Evaluate for Plasmodium parasites.
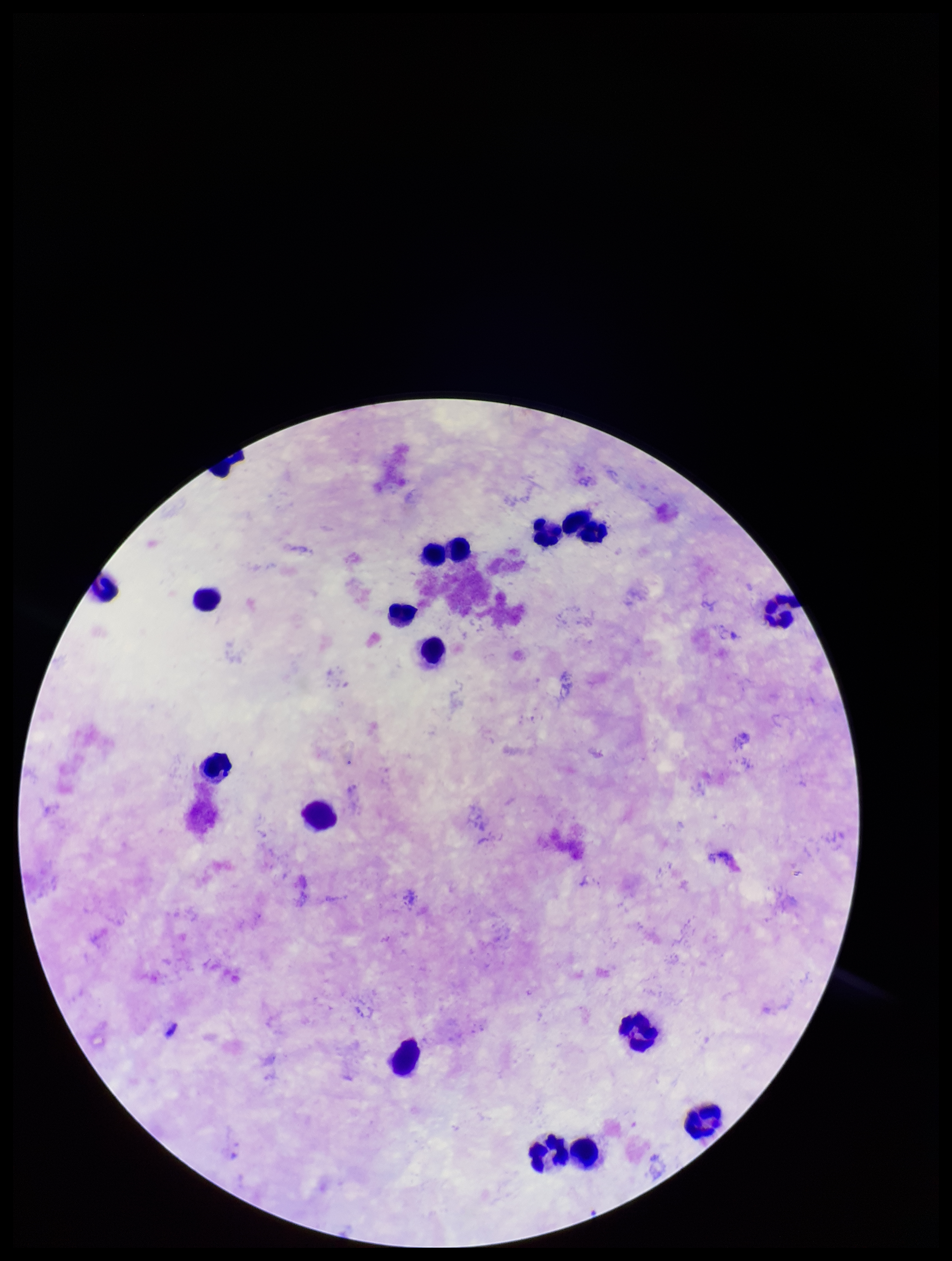
None seen.

Parasite count: 0. Leukocyte count: 16. Photographed through the microscope eyepiece with a smartphone camera. Single field of view. Preparation: thick. Image is 952×1261 pixels. Patient malaria status: negative. Stained with Giemsa.